Locate every Plasmodium parasite.
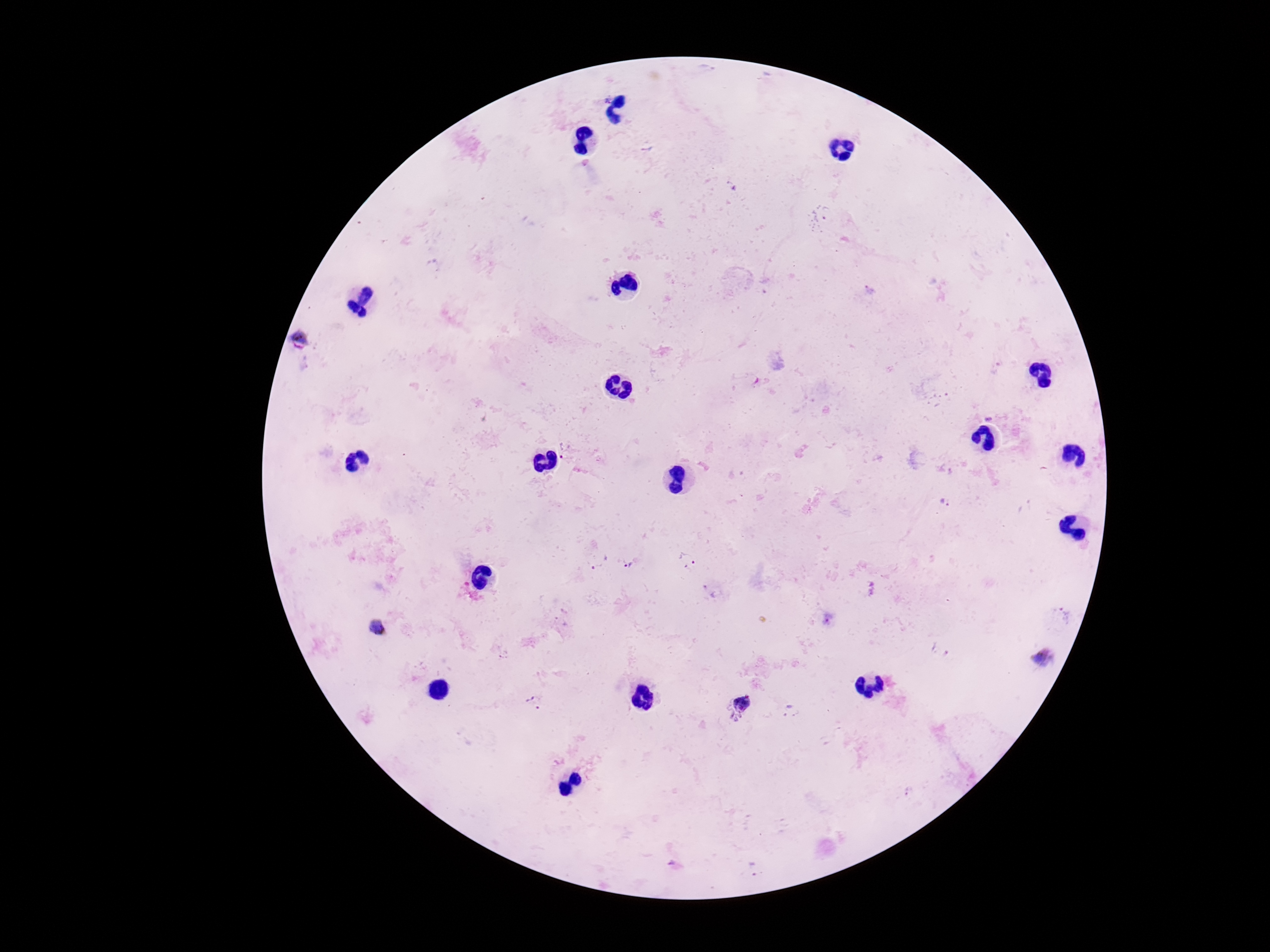
Approximate centers as [x, y] in pixels.
Plasmodium parasites: [606, 100], [300, 340], [565, 450], [947, 503], [598, 560], [689, 560], [630, 564], [708, 590], [561, 622], [377, 628], [940, 651], [1045, 659], [534, 702], [739, 704], [788, 712], [912, 792], [754, 867].

Image is 1270×952 pixels. Patient malaria status: infected. Single field of view. 100x magnification. Photographed through the microscope eyepiece with a smartphone camera. Thick peripheral-blood smear. Giemsa-stained preparation.